Assess this cell for malaria.
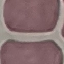

It is uninfected.

Summary:
  - Preparation: thin smear
  - Image type: cell patch, automatically extracted from a larger field of view and resized to 64 × 64 pixels
  - Capture: smartphone camera at the microscope eyepiece
  - Stain: Giemsa